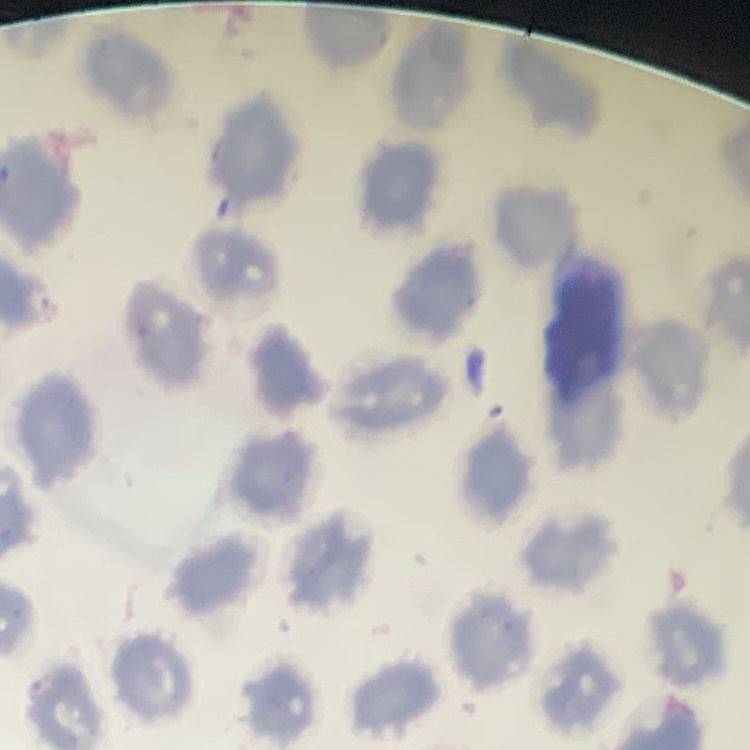
Summary:
  - Erythrocyte morphology: no rouleaux formation
  - Preparation: thin peripheral smear
  - Image type: square crop of a larger photomicrograph
  - Stain: Field's or Giemsa